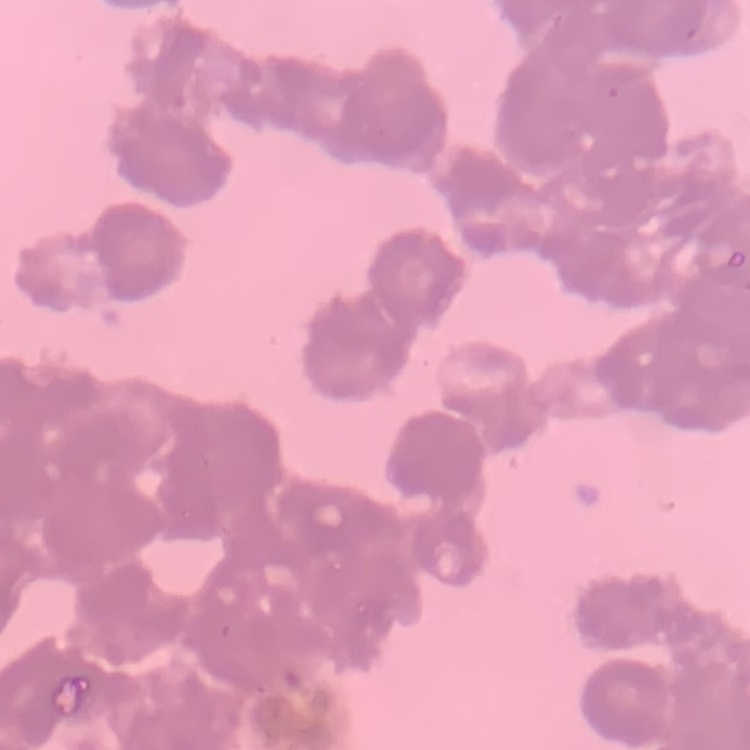
erythrocyte_morphology: rouleaux formation
image_type: one tile cut from a larger photomicrograph
stain: Field's or Giemsa
preparation: thin blood film